Report the malaria status of this cell.
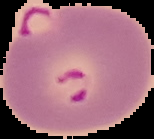
It is parasitized.

The area outside the segmented cell region is set to black. From a thin blood smear. Image is 154×139 pixels.